Comment on the morphology of the red blood cells.
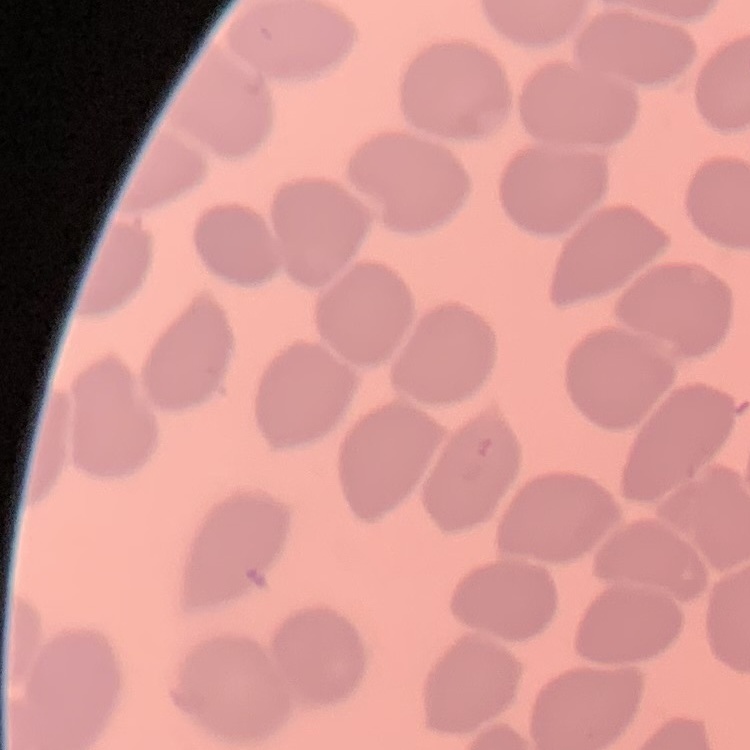

No rouleaux formation.

image type = square crop of a larger photomicrograph
preparation = thin blood film
stain = Field's or Giemsa